Comment on the morphology of the erythrocytes.
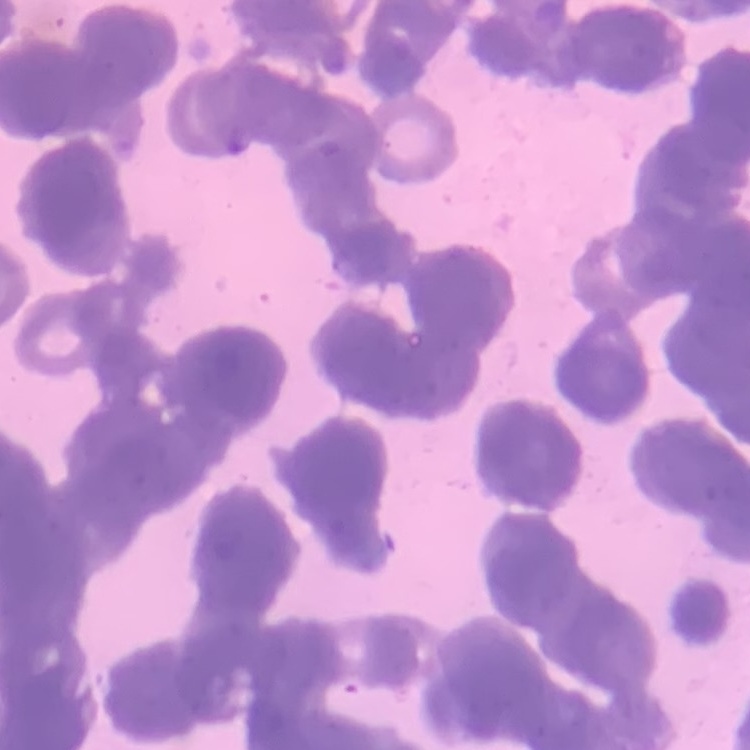

Rouleaux formation.

stain = Field's or Giemsa
preparation = thin peripheral smear
image type = one tile cut from a larger photomicrograph